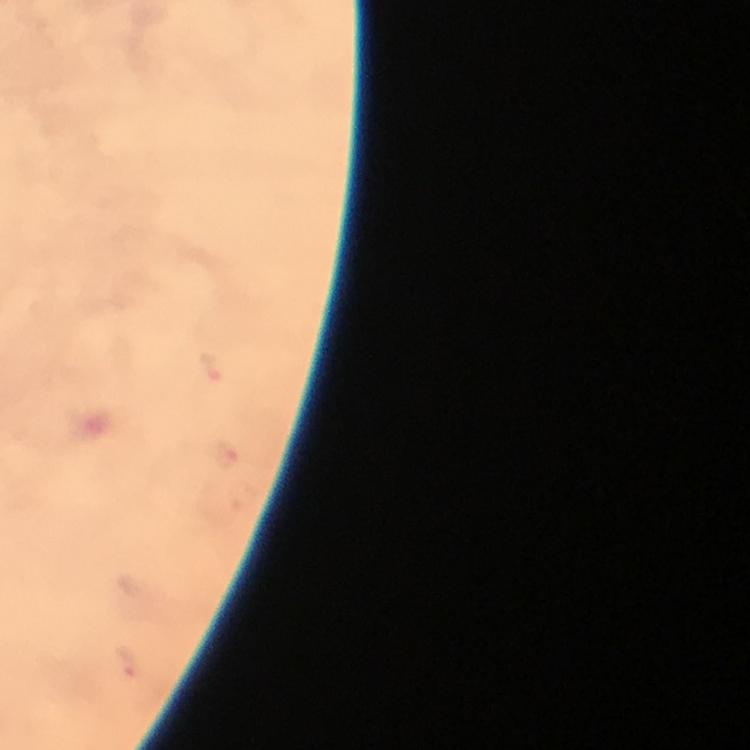
preparation: thick blood smear
image_size: 750×750 pixels
capture: smartphone camera through the microscope
immersion_oil: used
stain: Giemsa
context: from a diagnostic examination for malaria
magnification: 100x
plasmodium_parasite_locations: 'approximate centers as {x, y} in pixels: {211, 367}, {225, 453}, {129, 663}'
cropped_from: one field of view